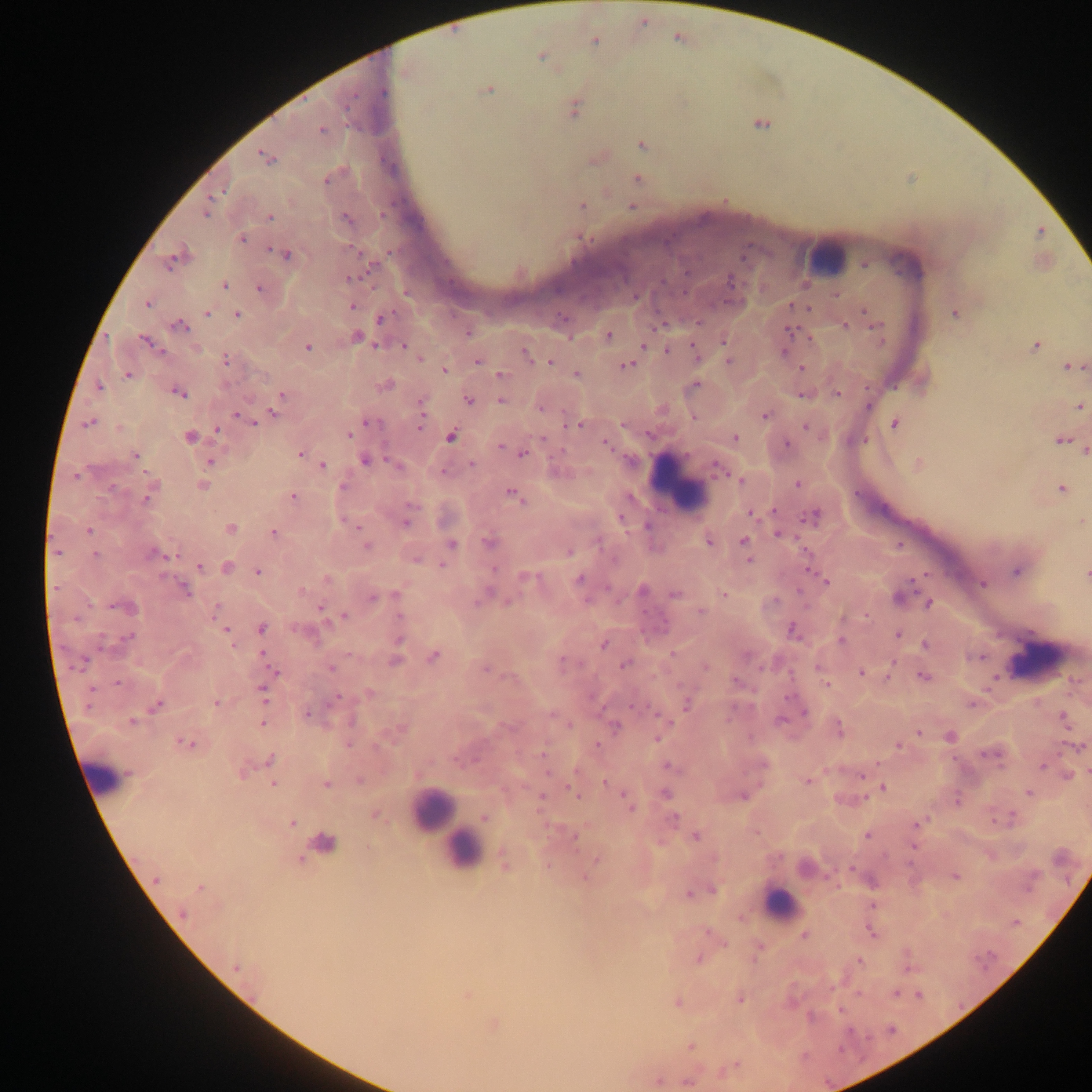
leukocyte_locations: 'approximate centers as [x, y] in pixels: [820, 258], [681, 484], [1037, 650], [109, 774], [448, 827], [780, 905]'
country: Ghana
plasmodium_parasite_locations: 'approximate centers as [x, y] in pixels: [679, 38], [488, 89], [355, 92], [383, 92], [760, 124], [640, 144], [261, 155], [325, 181], [224, 191], [581, 207], [206, 215], [269, 216], [348, 220], [240, 238], [282, 252], [175, 254], [290, 255], [171, 261], [864, 264], [367, 269], [685, 273], [361, 274], [664, 282], [732, 282], [225, 285], [260, 288], [686, 291], [835, 295], [147, 304], [790, 305], [352, 306], [808, 307], [863, 309], [207, 314], [236, 315], [563, 317], [383, 319], [699, 323], [181, 324], [846, 324], [876, 326], [790, 329], [608, 333], [810, 338], [144, 339], [725, 339], [880, 341], [377, 344], [691, 345], [1035, 345], [403, 346], [642, 346], [307, 347], [784, 350], [667, 351], [522, 352], [727, 359], [226, 360], [419, 360], [478, 362], [550, 362], [629, 364], [1066, 366], [801, 367], [1083, 367], [444, 371], [128, 375], [499, 375], [576, 375], [697, 385], [99, 386], [177, 392], [836, 392], [282, 394], [802, 394], [183, 395], [421, 400], [468, 400], [499, 400], [867, 406], [1080, 406], [273, 411], [238, 414], [422, 415], [765, 415], [367, 421], [255, 422], [894, 423], [87, 424], [565, 424], [581, 425], [622, 425], [361, 427], [805, 427], [419, 428], [217, 429], [349, 434], [452, 435], [186, 437], [734, 437], [543, 439], [865, 440], [1060, 441], [605, 442], [786, 443], [500, 446], [1083, 451], [523, 454], [136, 455], [300, 455], [624, 456], [364, 459], [387, 459], [209, 461], [473, 464], [714, 464], [918, 464], [323, 466], [147, 473], [729, 473], [75, 475], [737, 478], [741, 481], [797, 483], [344, 486], [112, 488], [1059, 488], [511, 493], [857, 493], [293, 496], [146, 498], [519, 499], [407, 504], [773, 509], [750, 514], [621, 518], [803, 518], [405, 523], [358, 527], [230, 528], [89, 529], [777, 532], [273, 533], [707, 540], [742, 540], [452, 543], [486, 543], [898, 543], [366, 546], [151, 551], [55, 552], [569, 553], [96, 554], [168, 556], [417, 558], [748, 560], [441, 564], [200, 566], [494, 569], [256, 570], [924, 574], [1085, 574], [521, 576], [579, 578], [326, 579], [910, 582], [826, 583], [983, 583], [183, 588], [911, 589], [798, 590], [303, 591], [187, 592], [395, 594], [675, 594], [725, 595], [372, 596], [775, 599], [508, 602], [477, 603], [928, 604], [89, 606], [113, 606], [216, 606], [320, 607], [700, 611], [645, 612], [214, 614], [344, 615], [399, 615], [865, 615], [262, 628], [227, 630], [792, 630], [897, 633], [129, 636], [841, 640], [399, 641], [604, 645], [924, 645], [233, 646], [262, 652], [348, 654], [671, 654], [433, 657], [980, 657], [85, 660], [562, 660], [893, 661], [395, 662], [623, 665], [760, 667], [74, 668], [331, 668], [486, 668], [862, 672], [275, 673], [921, 675], [888, 679], [735, 681], [118, 683], [826, 686], [91, 688], [261, 689], [337, 695], [788, 697], [264, 699], [214, 703], [686, 704], [158, 705], [972, 705], [1038, 705], [88, 706], [632, 706], [307, 713], [803, 713], [1061, 713], [656, 714], [552, 715], [726, 717], [1062, 718], [781, 720], [131, 721], [672, 721], [262, 724], [568, 726], [616, 727], [918, 732], [657, 738], [178, 741], [193, 744], [348, 745], [596, 745], [374, 747], [897, 747], [1060, 752], [541, 753], [983, 755], [270, 758], [953, 759], [453, 760], [876, 763], [1041, 767], [245, 771], [547, 774], [417, 775], [862, 775], [1066, 775], [359, 781], [605, 782], [807, 782], [274, 783], [326, 784], [567, 786], [883, 788], [572, 790], [622, 794], [1028, 794], [542, 797], [577, 797], [744, 797], [865, 797], [860, 800], [957, 801], [631, 809], [375, 815], [1013, 815], [484, 817], [675, 818], [992, 822], [291, 824], [917, 825], [755, 834], [696, 836], [866, 837], [574, 838], [658, 842], [913, 848], [989, 855], [596, 858], [505, 864], [850, 868], [584, 876], [825, 876], [954, 877], [155, 881], [838, 885], [713, 890], [1028, 891], [688, 892], [871, 905], [183, 914], [740, 918], [868, 930], [705, 931], [872, 933], [803, 935], [725, 944], [758, 945], [698, 959], [753, 960], [860, 961], [907, 968], [831, 990], [895, 992], [919, 994], [858, 995], [740, 1000], [677, 1002], [840, 1011], [891, 1031], [869, 1039], [689, 1046], [736, 1063], [721, 1073], [658, 1081], [683, 1081]'
preparation: thick blood film
capture: mobile-phone photograph through a microscope
field_of_view: single
image_size: 1092×1092 pixels